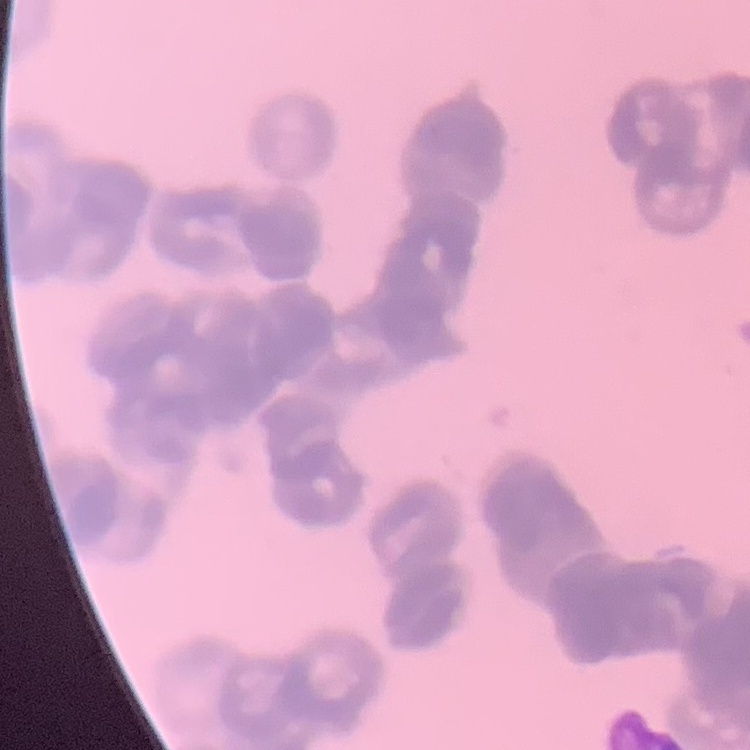

Summary:
  - Erythrocyte morphology: rouleaux formation
  - Image type: one tile cut from a larger photomicrograph
  - Stain: Field's or Giemsa
  - Preparation: thin blood smear